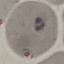

result: malaria parasites detected
stain: Giemsa
preparation: thin blood smear
capture: smartphone camera at the microscope eyepiece
image_type: cell patch, automatically extracted from a larger field of view and resized to 64 × 64 pixels